Assess the morphology of the erythrocytes.
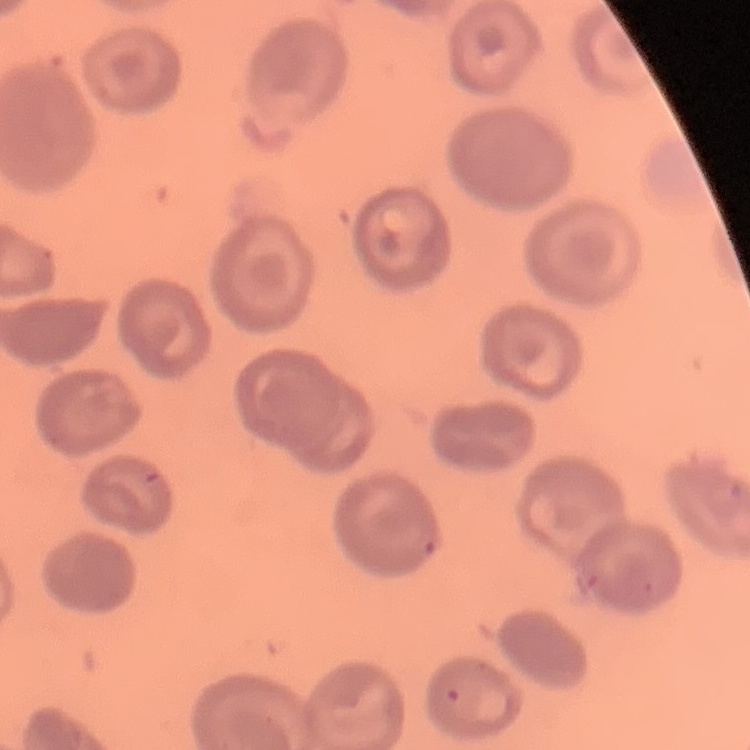
They show no rouleaux formation.

Summary:
  - Preparation: thin blood film
  - Stain: Field's or Giemsa
  - Image type: one tile cut from a larger photomicrograph